Report the malaria status of this cell.
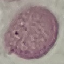

Uninfected.

Giemsa-stained preparation. Automatically extracted cell patch, resized to 64 × 64 pixels. Thin blood film. Photographed with a smartphone camera at the microscope eyepiece.